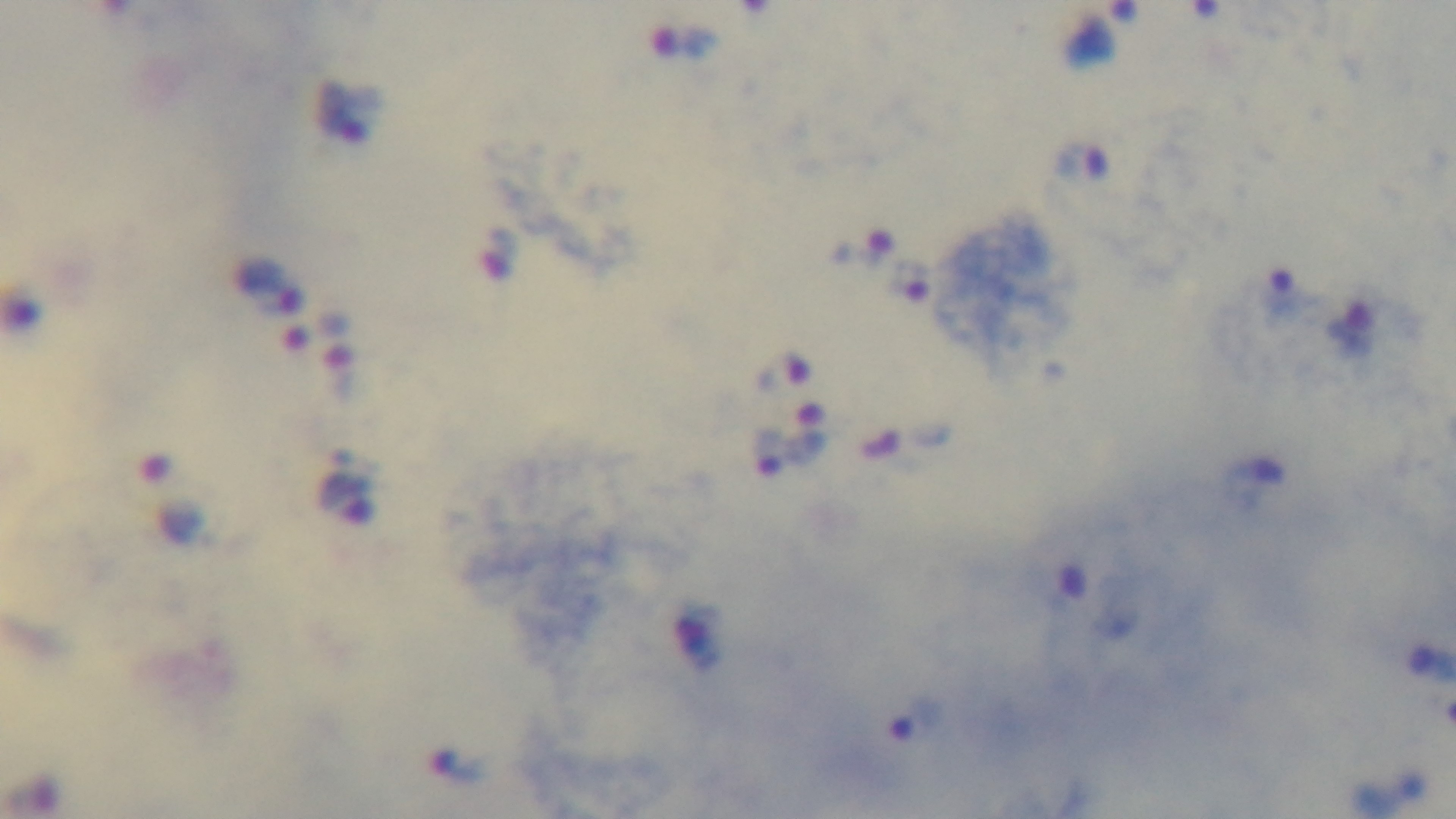

Preparation: thick blood film. Oil-immersion objective, 100x. Captured with a mounted 4K digital camera. Giemsa-stained. Malaria status: positive. Light microscopy. One field from the slide.